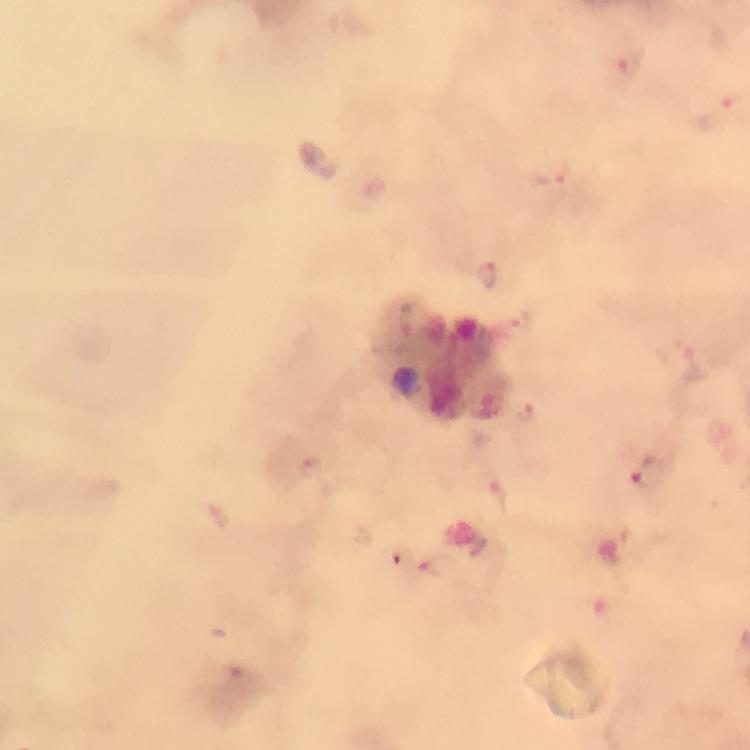
image size = 750×750 pixels
malaria parasite locations = approximate centers as (x, y) in pixels: (631, 63), (553, 173), (486, 274), (676, 354), (524, 412), (313, 469), (648, 471), (497, 501), (435, 565)
preparation = thick smear
stain = Giemsa
immersion oil = used
context = from a malaria diagnostic workup
cropped from = one field of view
capture = smartphone mounted on the microscope
magnification = 100x